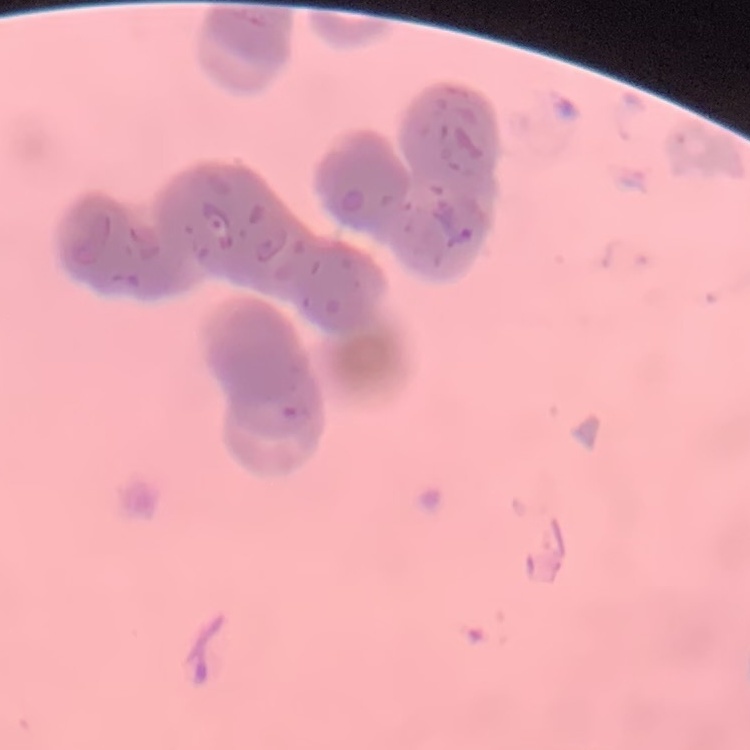

Summary:
  - Erythrocyte morphology: rouleaux formation
  - Preparation: thin blood film
  - Stain: Field's or Giemsa
  - Image type: one tile cut from a larger photomicrograph